Describe the morphology of the red blood cells.
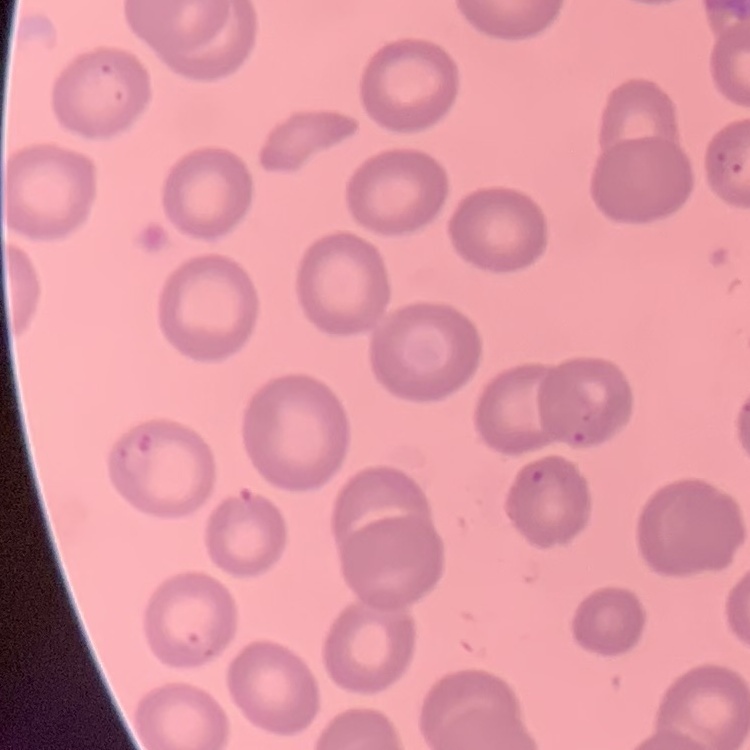
They show no rouleaux formation.

Stained with either Field's or Giemsa. Thin peripheral smear. One tile cut from a larger photomicrograph.